State the preparation type.
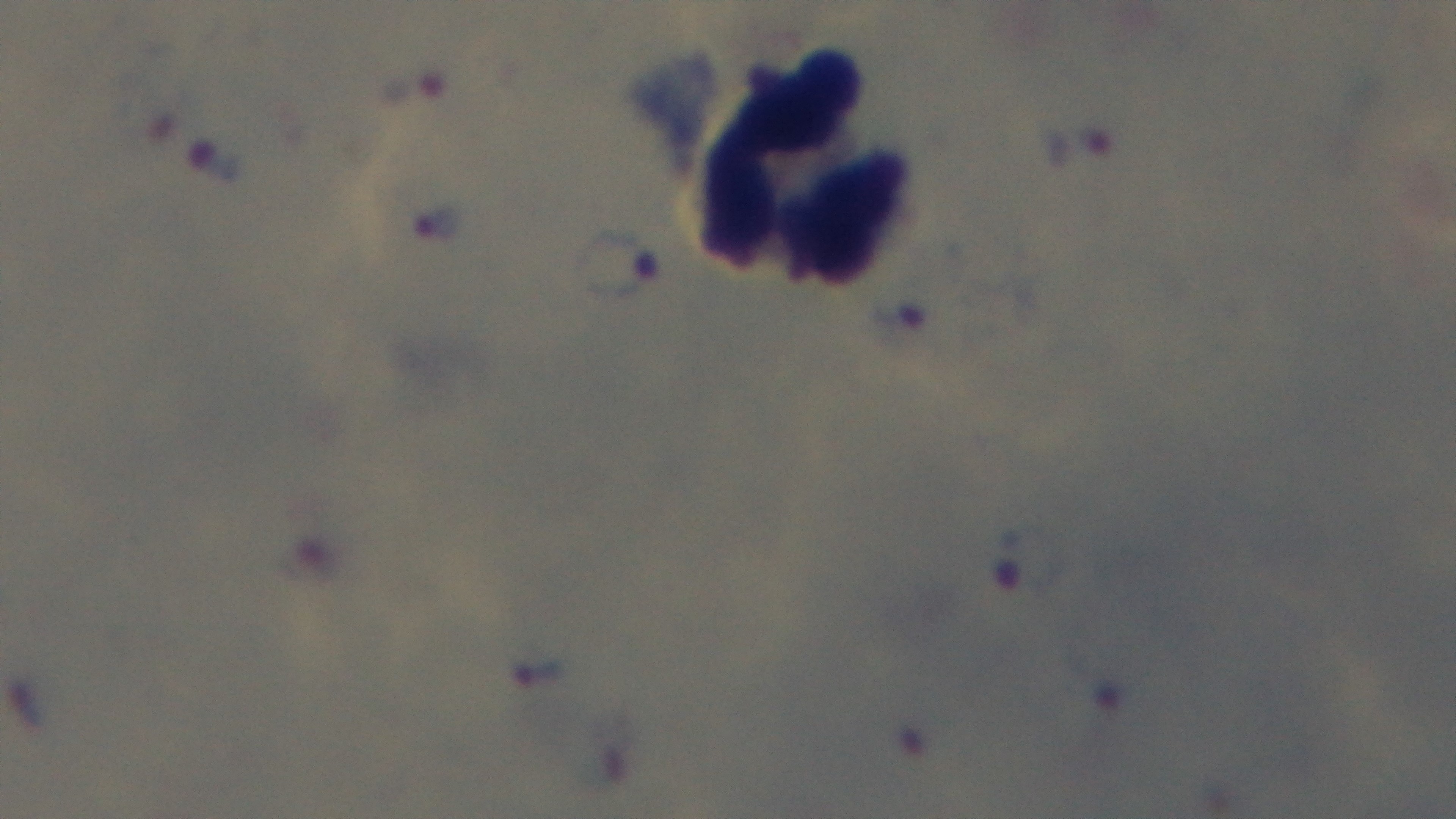
Thick.

{
  "capture": "mounted 4K digital camera",
  "stain": "Giemsa",
  "field_of_view": "single",
  "malaria_status": "positive",
  "modality": "light microscopy",
  "objective": "100x oil immersion"
}